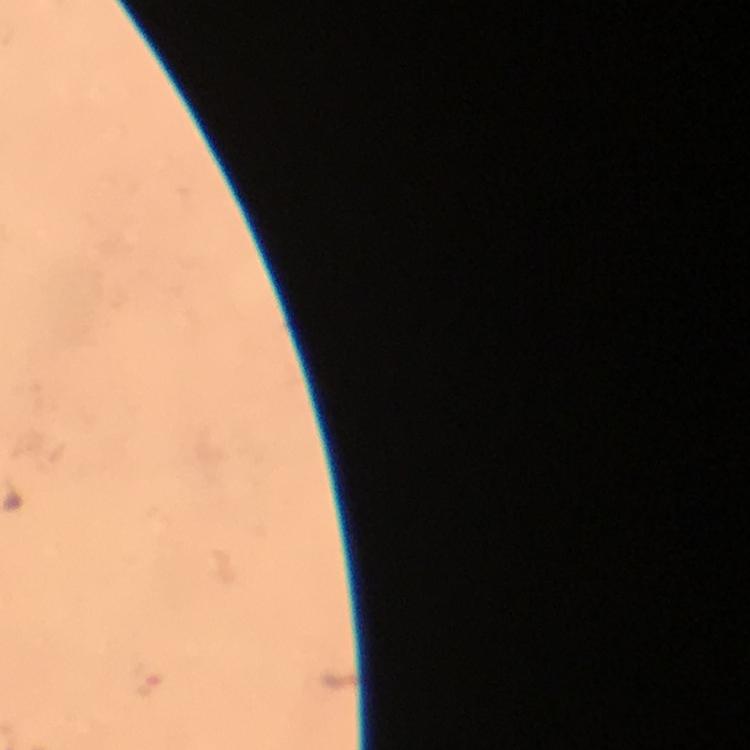
Approximate centers as [x, y] in pixels.
Summary:
  - Plasmodium parasite locations: [144, 681]
  - Preparation: thick blood film
  - Capture: smartphone photograph through a microscope
  - Context: from a diagnostic examination for malaria
  - Image size: 750×750 pixels
  - Immersion oil: applied
  - Stain: Giemsa
  - Magnification: 100x
  - Cropped from: one field of view